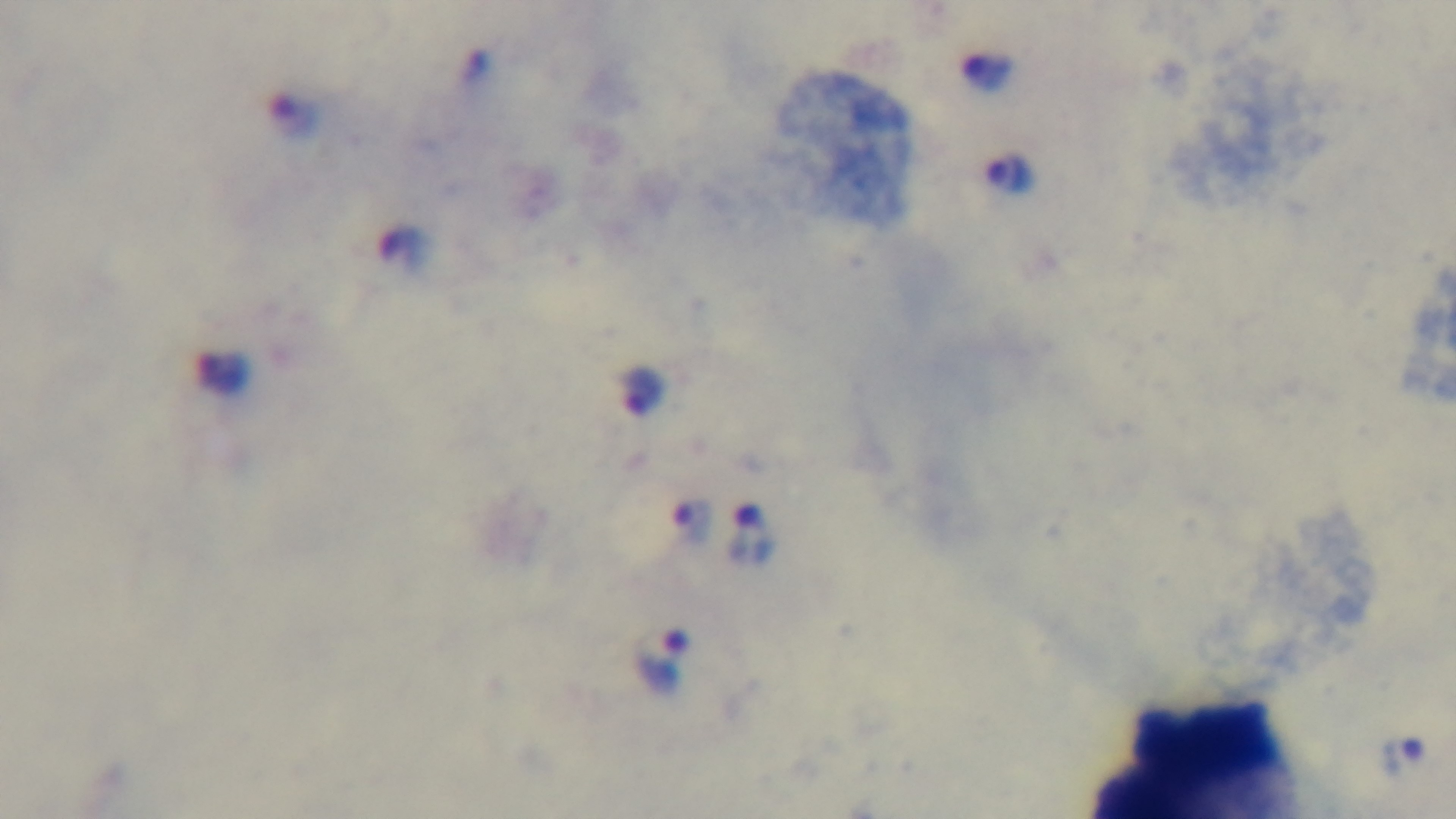
Summary:
  - Capture: mounted 4K digital camera
  - Stain: Giemsa
  - Objective: 100x oil immersion
  - Preparation: thick
  - Field of view: one from the slide
  - Malaria status: positive
  - Modality: light microscopy